Classify this cell by malaria status.
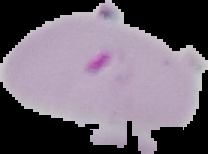

It is parasitized.

Image is 208×154 pixels. Cell region segmented out of the field of view; the surrounding area is masked to black. From a thin blood film.